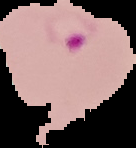

Summary:
  - Result: malaria parasites identified
  - Image size: 136×148 pixels
  - Image type: segmented cell region on a black background
  - Preparation: thin blood smear